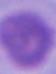

Summary:
  - Magnification: 1000x
  - Modality: micrograph
  - Identification: erythrocyte